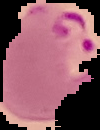
preparation = thin blood film
image size = 100×130 pixels
malaria status = parasitized
image type = cell region segmented out of the field of view; surrounding area masked to black